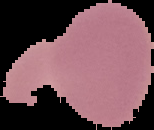
image_type: segmented cell region with the area outside set to black
image_size: 154×130 pixels
preparation: thin blood smear
malaria_status: uninfected